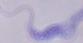

Summary:
  - Modality: micrograph
  - Identification: trypanosome
  - Magnification: 1000x